Report the malaria status of this cell.
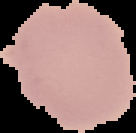

It is uninfected.

{
  "image_size": "136×133 pixels",
  "preparation": "thin blood film",
  "image_type": "cell region segmented out of the field of view; surrounding area masked to black"
}